Identify the parasite.
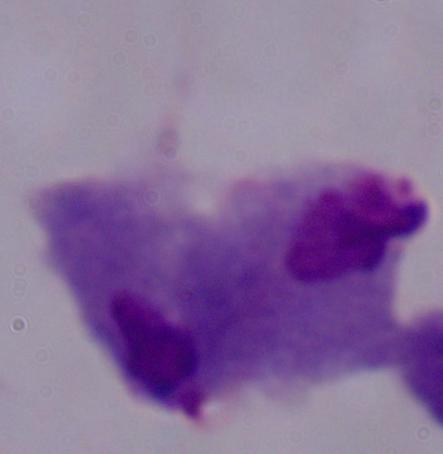
A trichomonad.

Micrograph. Captured at 1000x magnification.